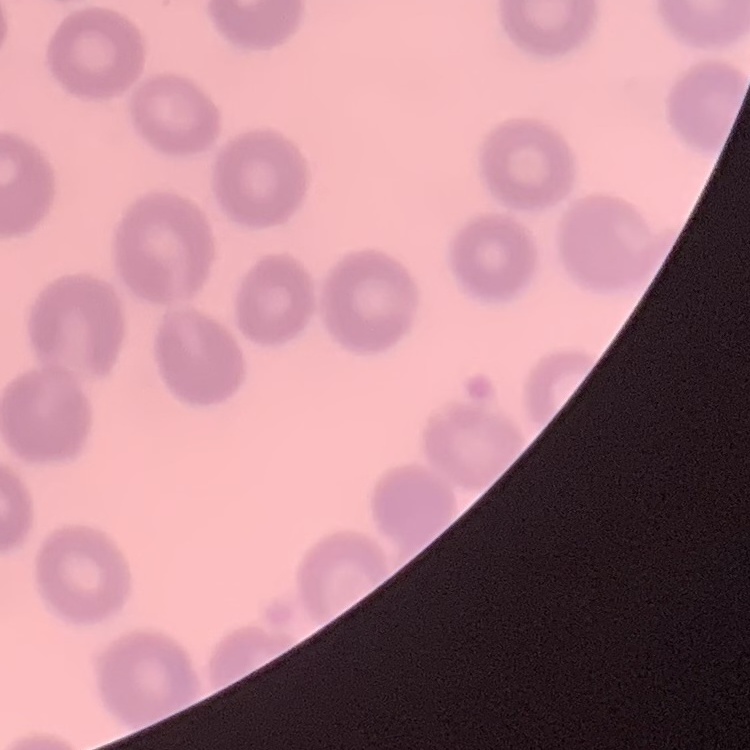
The erythrocytes show no rouleaux formation. One tile cut from a larger photomicrograph. Field's or Giemsa stain. Thin blood smear.